Assess this cell for malaria.
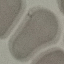
It is uninfected.

Thin blood film. Photographed with a smartphone camera at the microscope eyepiece. Cell patch, automatically extracted from a larger field of view and resized to 64 × 64 pixels. Giemsa-stained preparation.